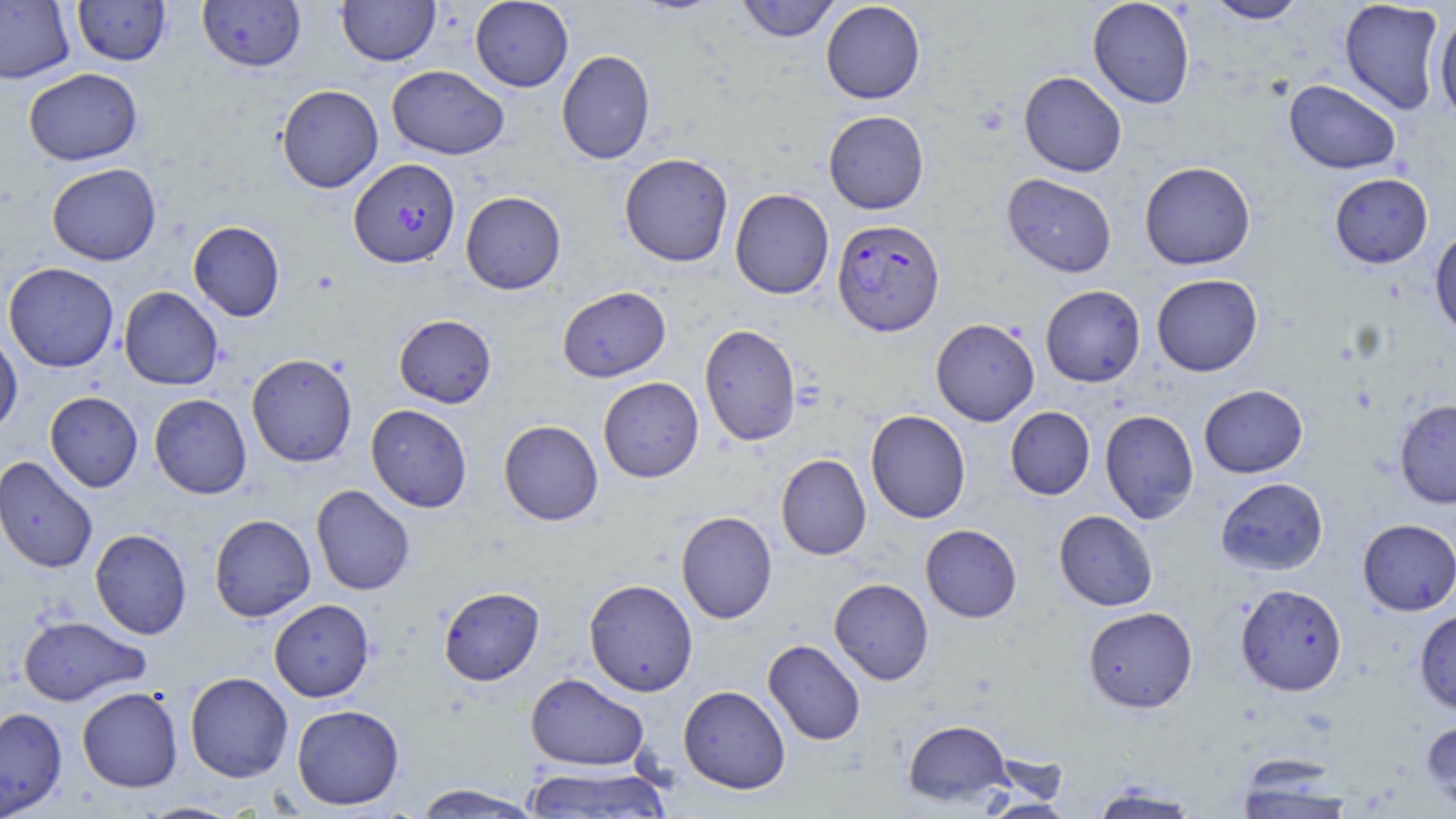

Summary:
  - Coordinate format: approximate bounding boxes as named x1/y1/x2/y2 corners in pixels
  - Uninfected red blood cell locations: (x1=72, y1=0, x2=171, y2=66), (x1=198, y1=0, x2=306, y2=72), (x1=336, y1=0, x2=439, y2=66), (x1=470, y1=0, x2=574, y2=92), (x1=736, y1=0, x2=840, y2=42), (x1=1087, y1=0, x2=1195, y2=109), (x1=1203, y1=0, x2=1310, y2=24), (x1=1339, y1=0, x2=1446, y2=115), (x1=0, y1=1, x2=75, y2=84), (x1=821, y1=1, x2=926, y2=104), (x1=1434, y1=14, x2=1456, y2=124), (x1=556, y1=49, x2=655, y2=164), (x1=387, y1=65, x2=509, y2=159), (x1=23, y1=68, x2=143, y2=166), (x1=1018, y1=71, x2=1127, y2=177), (x1=1284, y1=79, x2=1401, y2=174), (x1=276, y1=84, x2=383, y2=193), (x1=823, y1=110, x2=929, y2=214), (x1=619, y1=152, x2=733, y2=267), (x1=1139, y1=161, x2=1255, y2=270), (x1=46, y1=162, x2=162, y2=266), (x1=1002, y1=173, x2=1117, y2=277), (x1=1329, y1=173, x2=1433, y2=269), (x1=730, y1=188, x2=834, y2=299), (x1=460, y1=191, x2=566, y2=294), (x1=188, y1=221, x2=285, y2=322), (x1=1429, y1=226, x2=1456, y2=339), (x1=3, y1=262, x2=119, y2=373), (x1=1151, y1=273, x2=1263, y2=376), (x1=1040, y1=285, x2=1145, y2=387), (x1=119, y1=286, x2=223, y2=390), (x1=558, y1=286, x2=671, y2=382), (x1=393, y1=314, x2=496, y2=408), (x1=931, y1=318, x2=1040, y2=426), (x1=699, y1=323, x2=802, y2=447), (x1=0, y1=329, x2=23, y2=438), (x1=246, y1=353, x2=358, y2=468), (x1=598, y1=377, x2=704, y2=483), (x1=1198, y1=384, x2=1307, y2=478), (x1=45, y1=391, x2=143, y2=492), (x1=149, y1=394, x2=252, y2=498), (x1=1394, y1=399, x2=1456, y2=509), (x1=366, y1=404, x2=472, y2=513), (x1=1005, y1=406, x2=1095, y2=500), (x1=865, y1=410, x2=971, y2=523), (x1=1100, y1=410, x2=1199, y2=524), (x1=499, y1=419, x2=603, y2=525), (x1=776, y1=454, x2=871, y2=560), (x1=0, y1=456, x2=98, y2=574), (x1=1215, y1=477, x2=1328, y2=575), (x1=311, y1=484, x2=415, y2=596), (x1=1054, y1=510, x2=1158, y2=611), (x1=676, y1=511, x2=777, y2=624), (x1=209, y1=514, x2=316, y2=622), (x1=1357, y1=518, x2=1456, y2=615), (x1=920, y1=524, x2=1022, y2=622), (x1=90, y1=529, x2=192, y2=639), (x1=583, y1=578, x2=698, y2=696), (x1=829, y1=578, x2=933, y2=685), (x1=1235, y1=583, x2=1347, y2=696), (x1=438, y1=586, x2=544, y2=686), (x1=269, y1=599, x2=375, y2=702), (x1=1083, y1=606, x2=1198, y2=713), (x1=1414, y1=608, x2=1456, y2=716), (x1=17, y1=615, x2=150, y2=706), (x1=763, y1=639, x2=866, y2=746), (x1=185, y1=671, x2=293, y2=782), (x1=525, y1=673, x2=650, y2=771), (x1=678, y1=685, x2=791, y2=794), (x1=77, y1=686, x2=183, y2=793), (x1=291, y1=704, x2=405, y2=810), (x1=0, y1=707, x2=67, y2=816), (x1=1421, y1=717, x2=1456, y2=813), (x1=902, y1=719, x2=1012, y2=806), (x1=523, y1=764, x2=673, y2=818), (x1=1234, y1=767, x2=1355, y2=818), (x1=1089, y1=783, x2=1202, y2=819), (x1=411, y1=784, x2=543, y2=818), (x1=978, y1=798, x2=1078, y2=819), (x1=138, y1=801, x2=243, y2=819)
  - Plasmodium falciparum-infected red blood cell locations: (x1=348, y1=158, x2=460, y2=269), (x1=832, y1=218, x2=945, y2=335)
  - Slide-level diagnosis: Plasmodium falciparum
  - Magnification: 1000x
  - Field of view: single
  - Modality: optical microscopy
  - Preparation: thin blood film
  - Image size: 1456×819 pixels
  - Stain: May-Grünwald-Giemsa